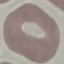
{
  "result": "no malaria parasites detected",
  "preparation": "thin smear",
  "image_type": "automatically extracted cell patch, resized to 64 × 64 pixels",
  "stain": "Giemsa",
  "capture": "smartphone camera at the microscope eyepiece"
}